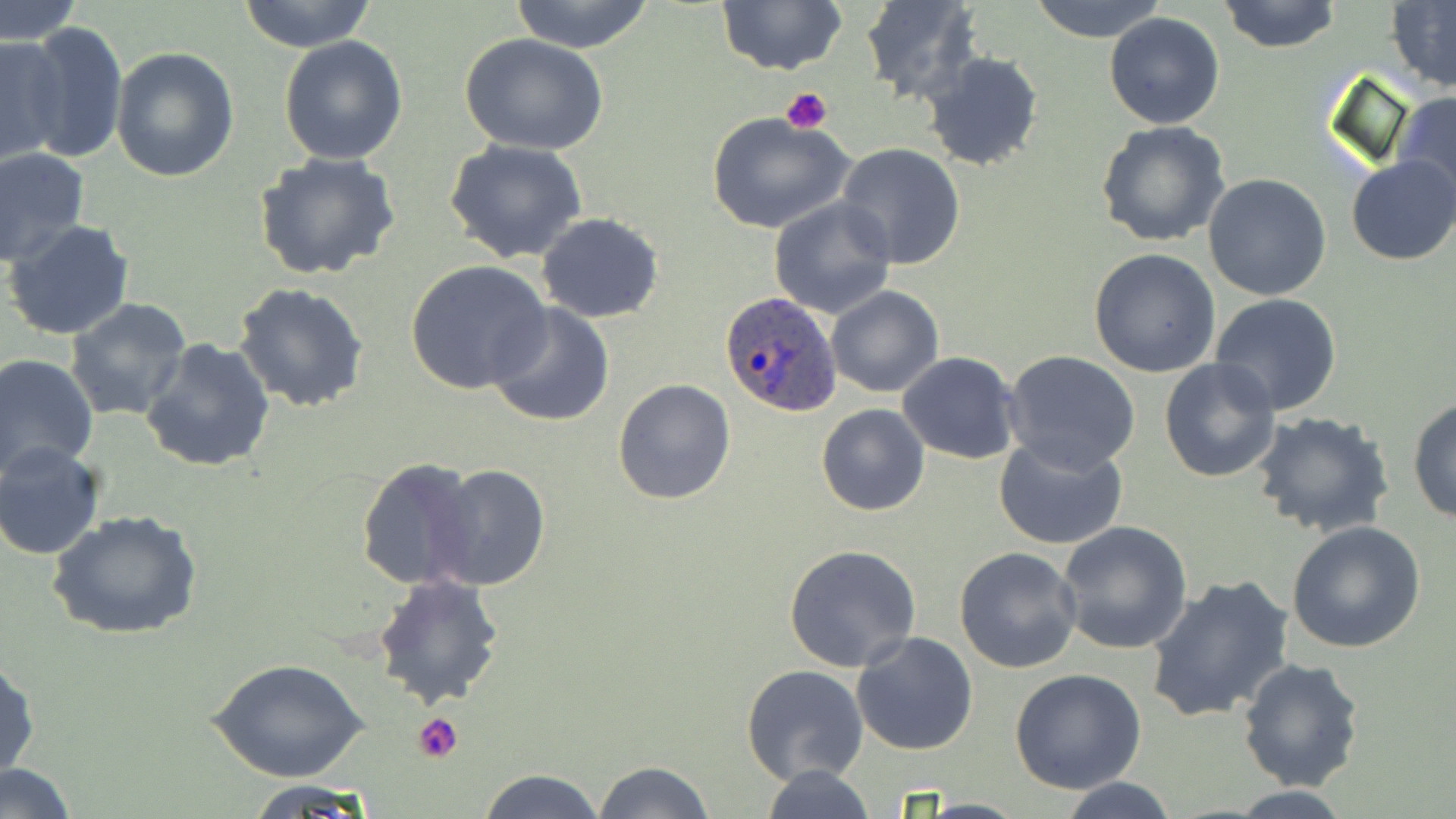
slide-level diagnosis = Plasmodium ovale
image size = 1456×819 pixels
platelet locations = approximate bounding boxes as (x1,y1)-(x2,y2) corner pairs in pixels: (780,86)-(834,135), (412,713)-(464,763)
modality = optical microscopy
preparation = thin blood smear
Plasmodium ovale-infected red blood cell locations = approximate bounding boxes as (x1,y1)-(x2,y2) corner pairs in pixels: (720,291)-(843,417)
field of view = single
stain = May-Grünwald-Giemsa
magnification = 1000x
uninfected red blood cell locations = approximate bounding boxes as (x1,y1)-(x2,y2) corner pairs in pixels: (238,0)-(378,52), (509,0)-(656,52), (862,0)-(982,105), (1029,0)-(1170,43), (1217,0)-(1343,54), (1,1)-(83,44), (716,1)-(846,76), (1386,2)-(1456,94), (1104,12)-(1225,129), (21,20)-(127,164), (0,35)-(69,167), (460,35)-(608,154), (279,36)-(408,165), (111,45)-(239,183), (922,50)-(1045,173), (1393,91)-(1456,212), (707,111)-(855,235), (1096,121)-(1232,248), (444,140)-(590,263), (835,144)-(966,268), (0,145)-(90,266), (253,153)-(403,283), (1347,155)-(1456,266), (1203,173)-(1333,301), (768,196)-(897,320), (537,213)-(665,323), (4,219)-(135,341), (1088,248)-(1221,377), (405,260)-(553,397), (233,282)-(369,413), (825,286)-(944,398), (1209,293)-(1344,417), (64,297)-(194,423), (485,301)-(617,428), (139,337)-(276,472), (1003,349)-(1142,473), (896,351)-(1020,463), (1,353)-(99,476), (1159,358)-(1283,483), (612,378)-(738,505), (1407,396)-(1456,525), (816,404)-(929,516), (1251,412)-(1395,539), (993,436)-(1128,554), (0,441)-(106,561), (353,458)-(481,592), (428,463)-(549,591), (48,508)-(203,641), (1285,519)-(1428,653), (1057,520)-(1193,654), (783,543)-(922,671), (953,546)-(1084,673), (1144,573)-(1295,725), (371,574)-(506,709), (851,632)-(980,756), (0,655)-(39,785), (1237,658)-(1367,792), (208,659)-(369,783), (741,666)-(870,786), (1009,669)-(1148,792), (592,760)-(717,819), (2,763)-(77,817), (756,764)-(880,819), (475,768)-(605,819), (1058,778)-(1182,818), (244,779)-(379,815), (1220,786)-(1363,817)